Comment on the morphology of the erythrocytes.
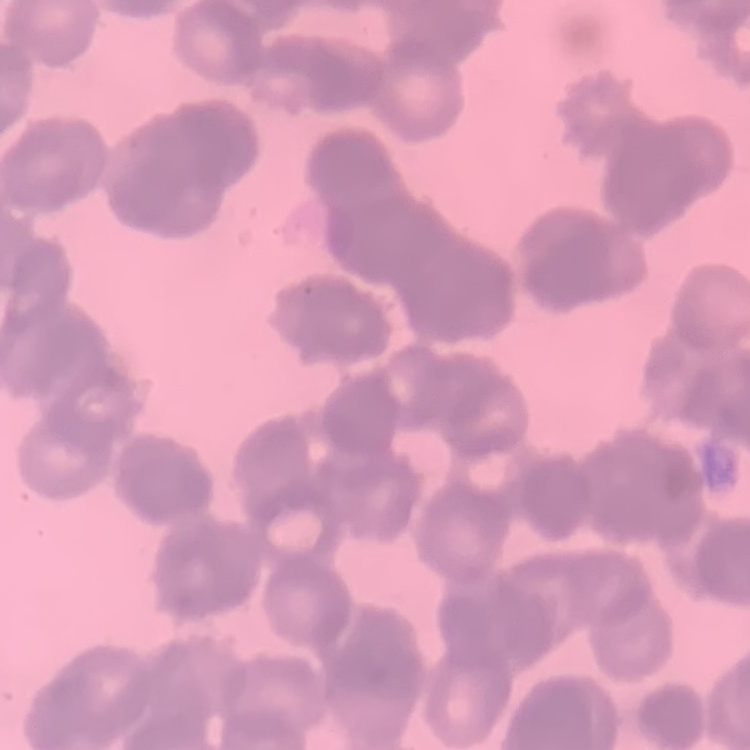

Rouleaux formation.

Summary:
  - Stain: Field's or Giemsa
  - Preparation: thin peripheral smear
  - Image type: one tile cut from a larger photomicrograph